Assess this cell for malaria.
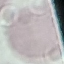

It is uninfected.

Acquired by smartphone through the microscope eyepiece. Giemsa-stained preparation. Cell patch, automatically extracted from a larger field of view and resized to 64 × 64 pixels. Thin blood smear.